Assess this cell for malaria.
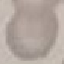
It is uninfected.

Automatically extracted cell patch, resized to 64 × 64 pixels. Giemsa stain. Acquired by smartphone through the microscope eyepiece. Thin smear of blood.